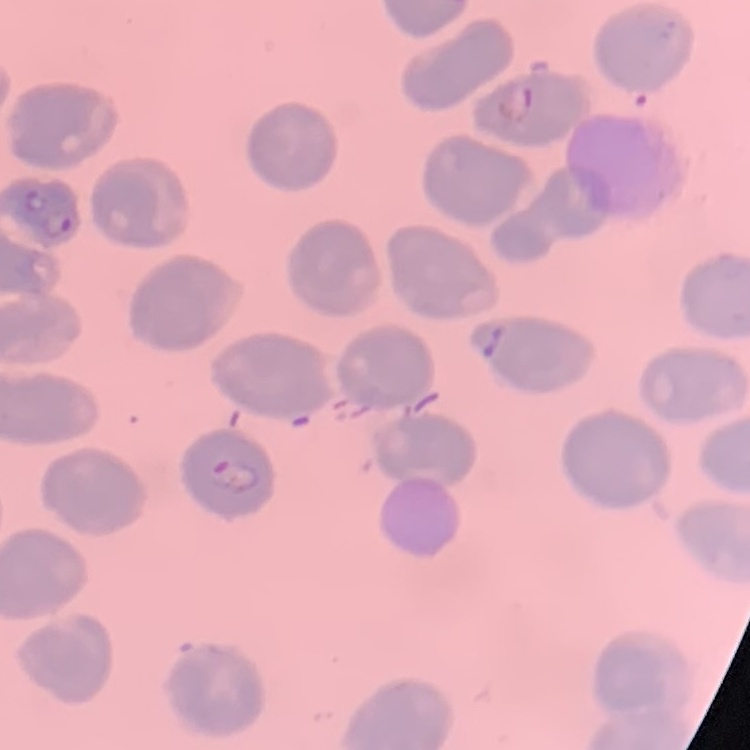

Summary:
  - Red blood cell morphology: no rouleaux formation
  - Stain: Field's or Giemsa
  - Preparation: thin peripheral smear
  - Image type: square crop of a larger photomicrograph